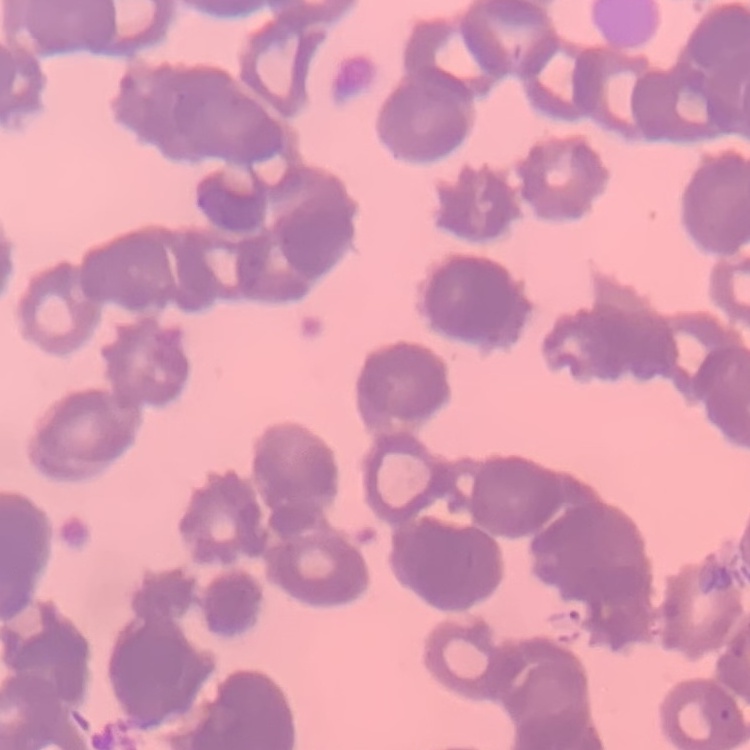

red_blood_cell_morphology: rouleaux formation
stain: Field's or Giemsa
preparation: thin blood film
image_type: one tile cut from a larger photomicrograph